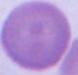
Summary:
  - Identification: erythrocyte
  - Magnification: 1000x
  - Modality: photomicrograph